Outline each Plasmodium ovale-infected red blood cell.
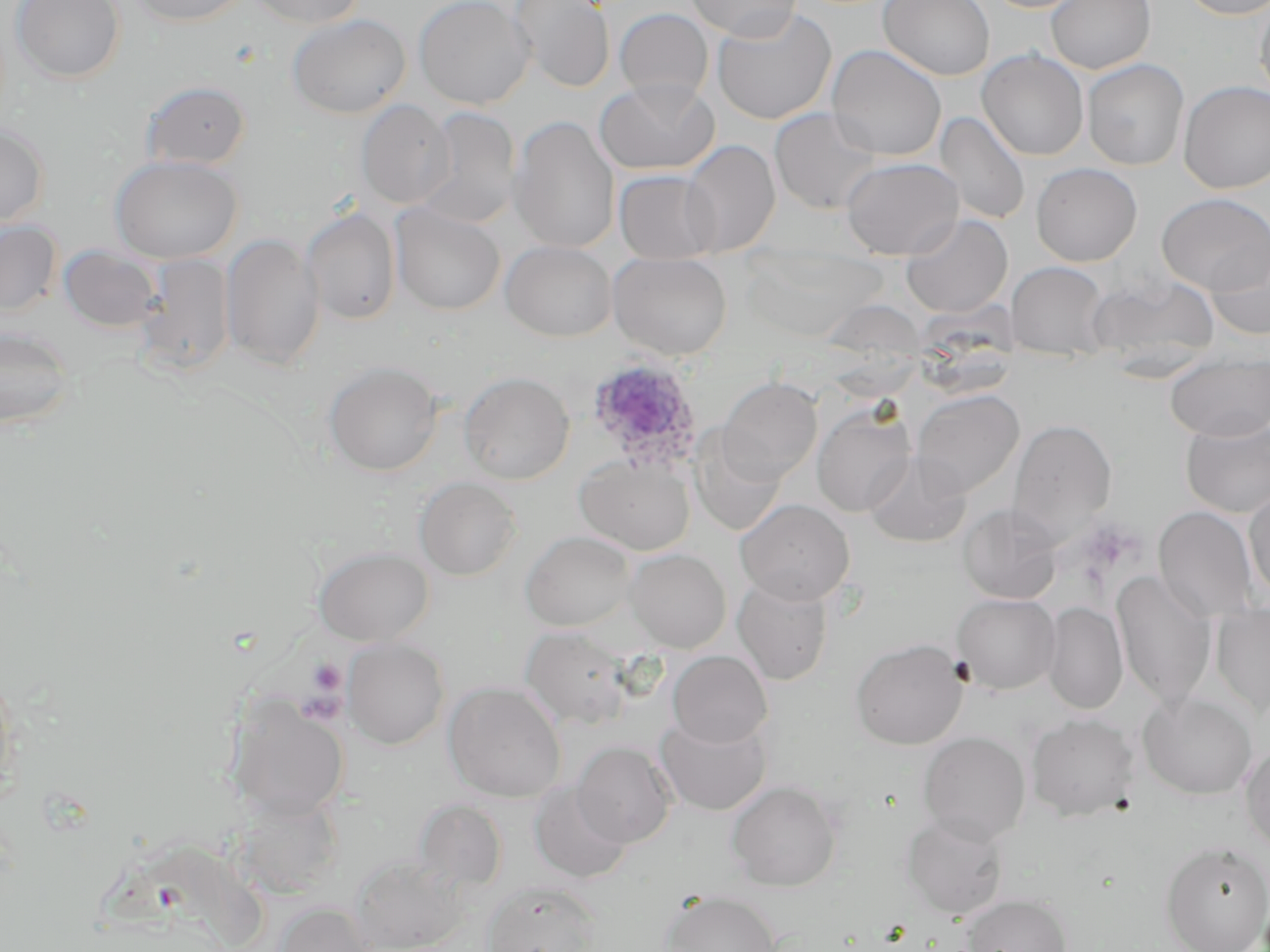

Approximate bounding boxes as named x1/y1/x2/y2 corners in pixels.
Plasmodium ovale-infected red blood cells: (x1=584, y1=358, x2=704, y2=473).

{
  "slide_level_diagnosis": "Plasmodium ovale",
  "preparation": "thin blood film",
  "magnification": "1000x",
  "uninfected_red_blood_cell_locations": "approximate bounding boxes as named x1/y1/x2/y2 corners in pixels: (x1=12, y1=0, x2=125, y2=83), (x1=128, y1=0, x2=248, y2=27), (x1=246, y1=0, x2=367, y2=28), (x1=414, y1=0, x2=535, y2=109), (x1=508, y1=0, x2=615, y2=93), (x1=683, y1=0, x2=803, y2=40), (x1=878, y1=0, x2=995, y2=81), (x1=983, y1=0, x2=1089, y2=13), (x1=1045, y1=0, x2=1156, y2=74), (x1=1179, y1=0, x2=1270, y2=20), (x1=1256, y1=2, x2=1270, y2=102), (x1=711, y1=6, x2=836, y2=125), (x1=614, y1=8, x2=713, y2=102), (x1=287, y1=13, x2=411, y2=118), (x1=826, y1=44, x2=947, y2=162), (x1=976, y1=49, x2=1089, y2=161), (x1=1082, y1=59, x2=1189, y2=171), (x1=594, y1=77, x2=719, y2=175), (x1=141, y1=80, x2=251, y2=170), (x1=1179, y1=81, x2=1270, y2=194), (x1=356, y1=99, x2=455, y2=209), (x1=415, y1=107, x2=521, y2=228), (x1=769, y1=107, x2=883, y2=215), (x1=935, y1=111, x2=1031, y2=226), (x1=508, y1=115, x2=620, y2=254), (x1=0, y1=124, x2=50, y2=228), (x1=679, y1=139, x2=780, y2=257), (x1=110, y1=154, x2=242, y2=264), (x1=840, y1=156, x2=963, y2=259), (x1=1031, y1=163, x2=1142, y2=266), (x1=614, y1=169, x2=720, y2=264), (x1=1157, y1=193, x2=1270, y2=295), (x1=390, y1=204, x2=505, y2=315), (x1=300, y1=207, x2=402, y2=325), (x1=900, y1=213, x2=1013, y2=318), (x1=0, y1=221, x2=62, y2=316), (x1=220, y1=232, x2=325, y2=370), (x1=1205, y1=239, x2=1270, y2=340), (x1=500, y1=240, x2=616, y2=342), (x1=59, y1=246, x2=162, y2=332), (x1=608, y1=252, x2=732, y2=360), (x1=135, y1=254, x2=235, y2=375), (x1=1006, y1=261, x2=1112, y2=361), (x1=1086, y1=271, x2=1220, y2=373), (x1=830, y1=304, x2=927, y2=399), (x1=0, y1=323, x2=79, y2=429), (x1=1166, y1=351, x2=1270, y2=441), (x1=324, y1=361, x2=443, y2=476), (x1=459, y1=371, x2=574, y2=485), (x1=719, y1=377, x2=822, y2=481), (x1=912, y1=389, x2=1025, y2=498), (x1=812, y1=405, x2=917, y2=517), (x1=1180, y1=416, x2=1270, y2=517), (x1=1009, y1=418, x2=1117, y2=539), (x1=691, y1=433, x2=788, y2=535), (x1=865, y1=452, x2=971, y2=548), (x1=574, y1=454, x2=695, y2=555), (x1=414, y1=476, x2=521, y2=580), (x1=1244, y1=486, x2=1270, y2=602), (x1=735, y1=498, x2=855, y2=605), (x1=958, y1=504, x2=1061, y2=604), (x1=1153, y1=506, x2=1258, y2=624), (x1=520, y1=530, x2=637, y2=632), (x1=313, y1=546, x2=434, y2=646), (x1=625, y1=548, x2=731, y2=652), (x1=1112, y1=571, x2=1216, y2=707), (x1=732, y1=575, x2=833, y2=685), (x1=952, y1=593, x2=1060, y2=694), (x1=1043, y1=601, x2=1128, y2=715), (x1=1211, y1=602, x2=1270, y2=716), (x1=520, y1=625, x2=634, y2=730), (x1=343, y1=638, x2=449, y2=750), (x1=850, y1=639, x2=968, y2=749), (x1=667, y1=650, x2=772, y2=748), (x1=0, y1=659, x2=22, y2=808), (x1=444, y1=681, x2=567, y2=803), (x1=1138, y1=692, x2=1257, y2=799), (x1=229, y1=696, x2=349, y2=820), (x1=655, y1=713, x2=772, y2=815), (x1=1027, y1=713, x2=1139, y2=821), (x1=918, y1=731, x2=1030, y2=844), (x1=572, y1=741, x2=677, y2=848), (x1=1240, y1=742, x2=1270, y2=855), (x1=529, y1=780, x2=633, y2=884), (x1=726, y1=780, x2=841, y2=891), (x1=232, y1=793, x2=345, y2=900), (x1=413, y1=800, x2=508, y2=893), (x1=901, y1=813, x2=1010, y2=919), (x1=1160, y1=841, x2=1270, y2=952), (x1=349, y1=855, x2=468, y2=952), (x1=482, y1=880, x2=600, y2=952), (x1=661, y1=890, x2=782, y2=952), (x1=962, y1=894, x2=1072, y2=952), (x1=273, y1=901, x2=377, y2=952)",
  "stain": "May-Grünwald-Giemsa",
  "field_of_view": "one of a larger specimen",
  "platelet_locations": "approximate bounding boxes as named x1/y1/x2/y2 corners in pixels: (x1=308, y1=658, x2=346, y2=695)",
  "image_size": "1270×952 pixels",
  "modality": "optical microscopy"
}